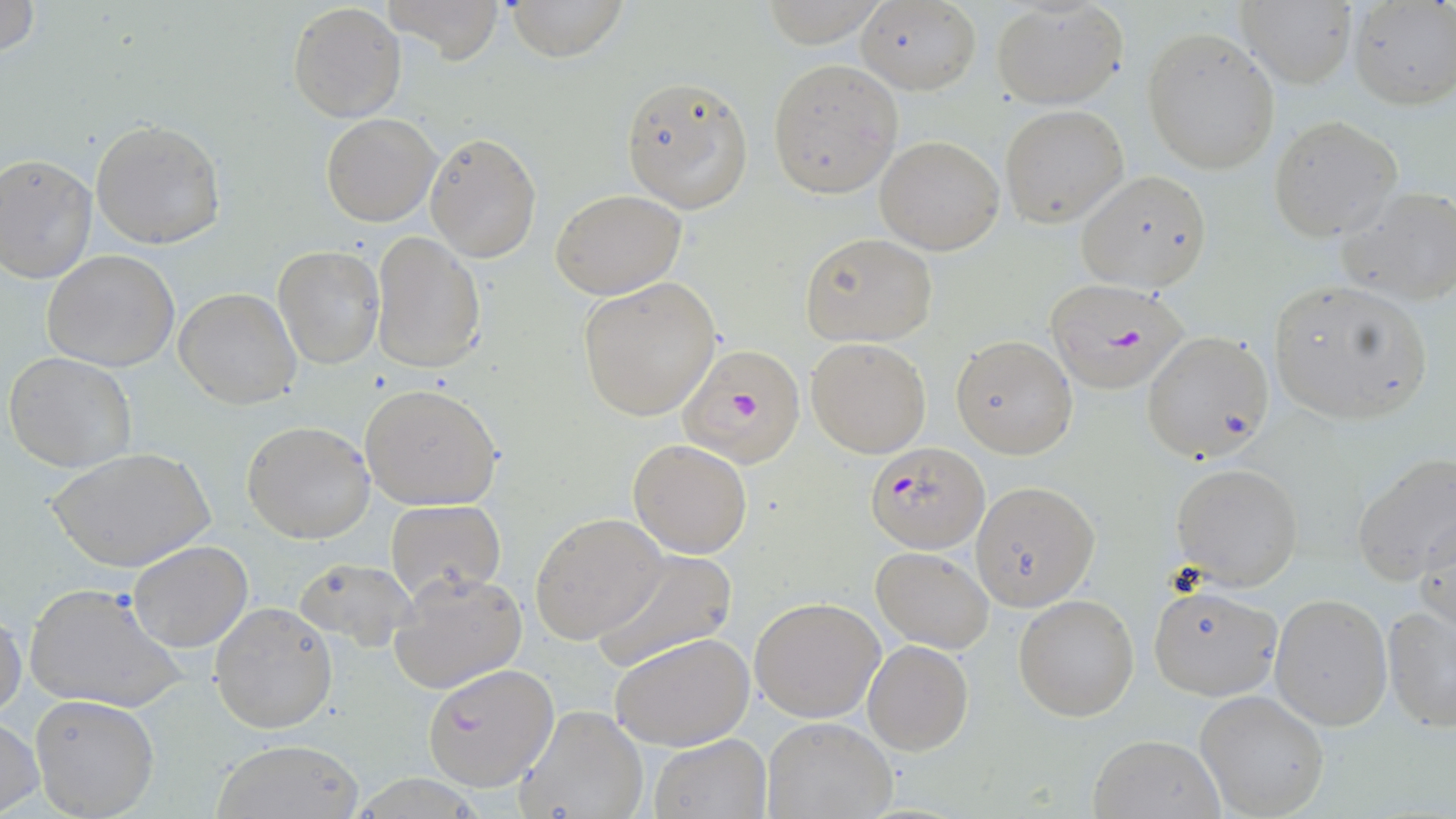

slide-level diagnosis = Plasmodium falciparum
magnification = 1000x
Plasmodium falciparum-infected red blood cell locations = approximate bounding boxes as (x1,y1)-(x2,y2) corner pairs in pixels: (1042,278)-(1191,394), (676,344)-(808,468), (865,441)-(990,553), (422,662)-(559,791)
modality = optical microscopy
uninfected red blood cell locations = approximate bounding boxes as (x1,y1)-(x2,y2) corner pairs in pixels: (0,0)-(41,60), (376,0)-(509,63), (510,0)-(625,61), (287,2)-(406,123), (854,2)-(982,94), (1239,2)-(1356,88), (1349,2)-(1455,110), (991,3)-(1127,109), (1142,27)-(1280,174), (767,60)-(903,198), (619,73)-(754,215), (999,104)-(1129,227), (319,112)-(440,226), (1267,116)-(1402,241), (90,119)-(225,249), (424,132)-(542,263), (875,135)-(1005,256), (0,154)-(97,284), (1075,170)-(1213,292), (1338,186)-(1456,304), (550,189)-(687,300), (372,231)-(486,376), (798,232)-(937,347), (274,244)-(384,369), (42,250)-(182,371), (577,276)-(723,421), (1266,278)-(1433,424), (174,287)-(302,410), (1141,330)-(1274,463), (950,335)-(1077,458), (806,336)-(931,457), (4,352)-(137,474), (358,382)-(503,512), (240,420)-(374,543), (628,438)-(752,558), (48,447)-(213,575), (1352,453)-(1456,586), (1173,461)-(1306,590), (970,479)-(1100,610), (384,499)-(505,602), (1415,509)-(1455,638), (530,512)-(666,647), (128,538)-(254,652), (590,546)-(739,671), (870,546)-(994,653), (292,556)-(415,653), (389,568)-(527,694), (1146,582)-(1282,702), (22,585)-(186,714), (1013,592)-(1141,721), (1271,593)-(1393,731), (750,596)-(884,722), (210,600)-(338,734), (1381,604)-(1455,733), (0,609)-(25,723), (610,632)-(755,751), (862,639)-(974,754), (1195,690)-(1329,819), (30,694)-(160,818), (512,702)-(649,819), (761,716)-(897,818), (0,717)-(43,817), (1087,732)-(1222,818), (650,733)-(771,818), (209,737)-(365,819)
stain = May-Grünwald-Giemsa
field of view = one of a larger specimen
preparation = thin blood smear
image size = 1456×819 pixels